Comment on the morphology of the erythrocytes.
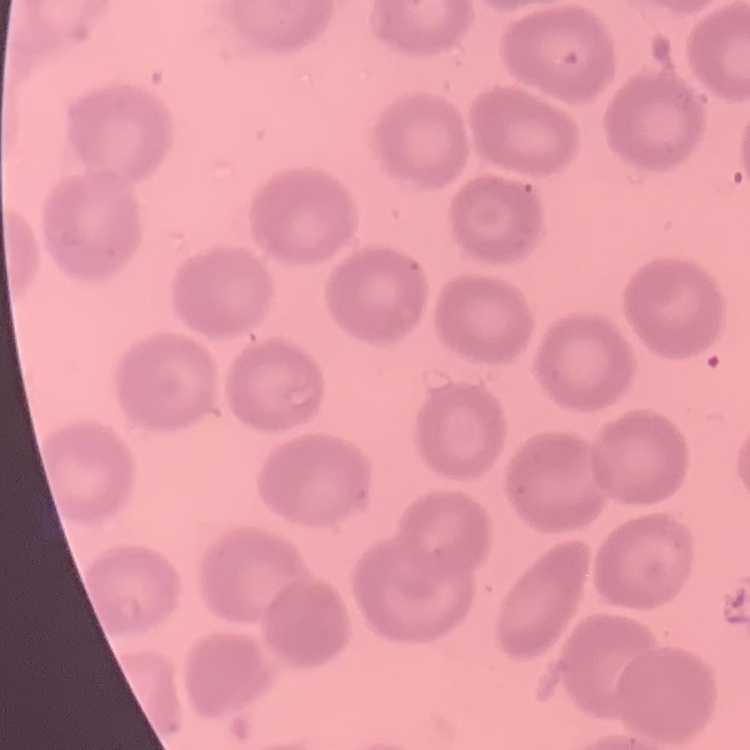
No rouleaux formation.

Thin blood film. Field's or Giemsa stain. Square crop of a larger photomicrograph.